Identify the parasite.
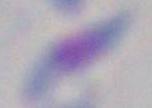

This is Toxoplasma gondii.

Summary:
  - Modality: micrograph
  - Magnification: 1000x